Comment on the morphology of the erythrocytes.
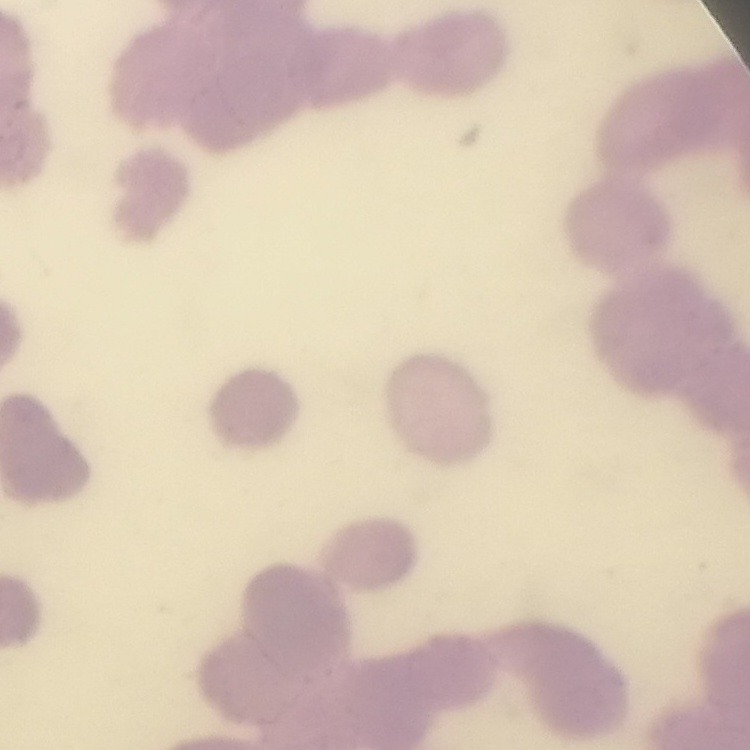

Rouleaux formation.

preparation = thin blood smear
image type = square crop of a larger photomicrograph
stain = Field's or Giemsa